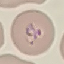 Result: malaria parasites identified. Acquired by smartphone through the microscope eyepiece. Automatically extracted cell patch, resized to 64 × 64 pixels. Thin smear of blood. Giemsa stain.